Outline each Plasmodium ovale-infected red blood cell.
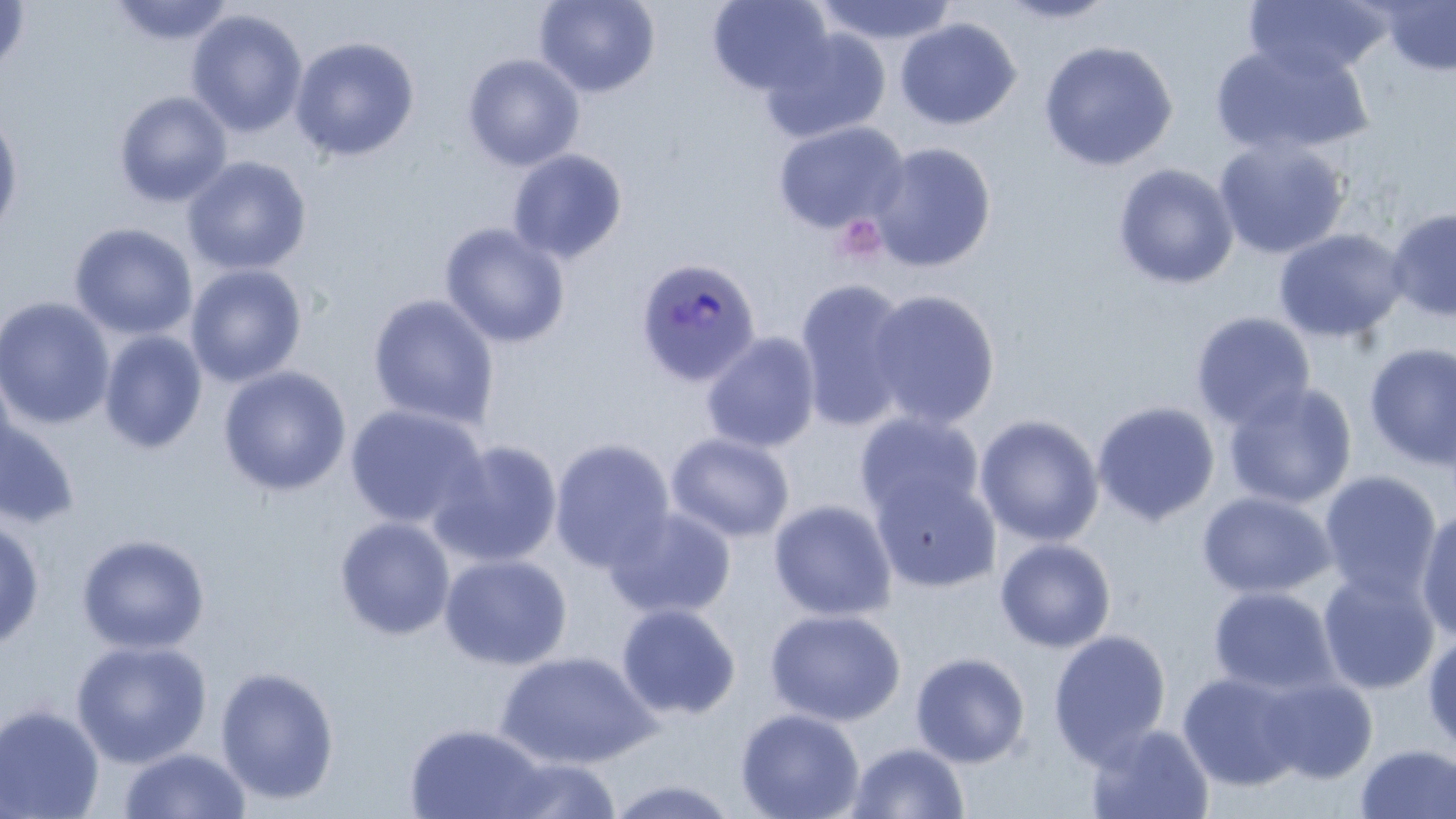

Approximate bounding boxes as named x1/y1/x2/y2 corners in pixels.
Plasmodium ovale-infected red blood cells: (x1=634, y1=257, x2=761, y2=387).

Platelet locations: (x1=832, y1=213, x2=887, y2=266). Uninfected red blood cell locations: (x1=0, y1=0, x2=31, y2=77), (x1=534, y1=0, x2=660, y2=98), (x1=707, y1=0, x2=833, y2=96), (x1=812, y1=0, x2=959, y2=46), (x1=995, y1=0, x2=1119, y2=25), (x1=1243, y1=0, x2=1390, y2=80), (x1=109, y1=1, x2=238, y2=46), (x1=1379, y1=1, x2=1456, y2=76), (x1=186, y1=10, x2=308, y2=138), (x1=895, y1=18, x2=1021, y2=131), (x1=760, y1=27, x2=891, y2=144), (x1=290, y1=37, x2=420, y2=162), (x1=1038, y1=40, x2=1178, y2=172), (x1=1210, y1=41, x2=1373, y2=158), (x1=462, y1=54, x2=584, y2=171), (x1=114, y1=91, x2=232, y2=208), (x1=0, y1=110, x2=24, y2=241), (x1=772, y1=121, x2=909, y2=234), (x1=1214, y1=138, x2=1350, y2=260), (x1=870, y1=142, x2=996, y2=272), (x1=507, y1=149, x2=628, y2=264), (x1=182, y1=155, x2=312, y2=276), (x1=1113, y1=163, x2=1238, y2=290), (x1=1386, y1=206, x2=1456, y2=323), (x1=439, y1=222, x2=571, y2=348), (x1=69, y1=223, x2=197, y2=339), (x1=1273, y1=228, x2=1409, y2=343), (x1=185, y1=263, x2=307, y2=387), (x1=793, y1=278, x2=914, y2=431), (x1=864, y1=289, x2=1000, y2=431), (x1=366, y1=294, x2=500, y2=430), (x1=0, y1=297, x2=116, y2=430), (x1=1191, y1=311, x2=1316, y2=430), (x1=98, y1=330, x2=208, y2=454), (x1=701, y1=332, x2=822, y2=453), (x1=1363, y1=343, x2=1456, y2=471), (x1=218, y1=366, x2=352, y2=497), (x1=1223, y1=382, x2=1357, y2=510), (x1=1092, y1=401, x2=1220, y2=526), (x1=344, y1=403, x2=488, y2=530), (x1=0, y1=411, x2=81, y2=530), (x1=854, y1=411, x2=985, y2=524), (x1=974, y1=414, x2=1104, y2=547), (x1=666, y1=432, x2=794, y2=543), (x1=549, y1=438, x2=676, y2=572), (x1=430, y1=439, x2=563, y2=568), (x1=871, y1=471, x2=1002, y2=593), (x1=1318, y1=471, x2=1442, y2=602), (x1=1197, y1=491, x2=1337, y2=600), (x1=768, y1=499, x2=897, y2=621), (x1=604, y1=507, x2=736, y2=620), (x1=1416, y1=507, x2=1456, y2=642), (x1=0, y1=514, x2=45, y2=651), (x1=334, y1=516, x2=456, y2=641), (x1=76, y1=533, x2=210, y2=654), (x1=994, y1=537, x2=1116, y2=653), (x1=439, y1=552, x2=573, y2=670), (x1=1317, y1=569, x2=1441, y2=695), (x1=1207, y1=586, x2=1341, y2=699), (x1=615, y1=603, x2=741, y2=721), (x1=765, y1=608, x2=906, y2=726), (x1=1422, y1=628, x2=1456, y2=756), (x1=1048, y1=630, x2=1171, y2=764), (x1=70, y1=639, x2=212, y2=768), (x1=494, y1=651, x2=659, y2=769), (x1=910, y1=651, x2=1031, y2=768), (x1=215, y1=665, x2=340, y2=804), (x1=1177, y1=672, x2=1306, y2=791), (x1=1257, y1=675, x2=1378, y2=783), (x1=0, y1=704, x2=105, y2=819), (x1=734, y1=708, x2=865, y2=819), (x1=1085, y1=722, x2=1215, y2=819), (x1=404, y1=723, x2=549, y2=818), (x1=846, y1=741, x2=970, y2=819), (x1=1355, y1=743, x2=1455, y2=819), (x1=117, y1=747, x2=252, y2=819), (x1=493, y1=756, x2=623, y2=818), (x1=603, y1=777, x2=743, y2=819). Slide-level diagnosis: Plasmodium ovale. May-Grünwald-Giemsa stain. Thin blood smear. Light microscopy. Single field of view. 1000x magnification. Image is 1456×819 pixels.